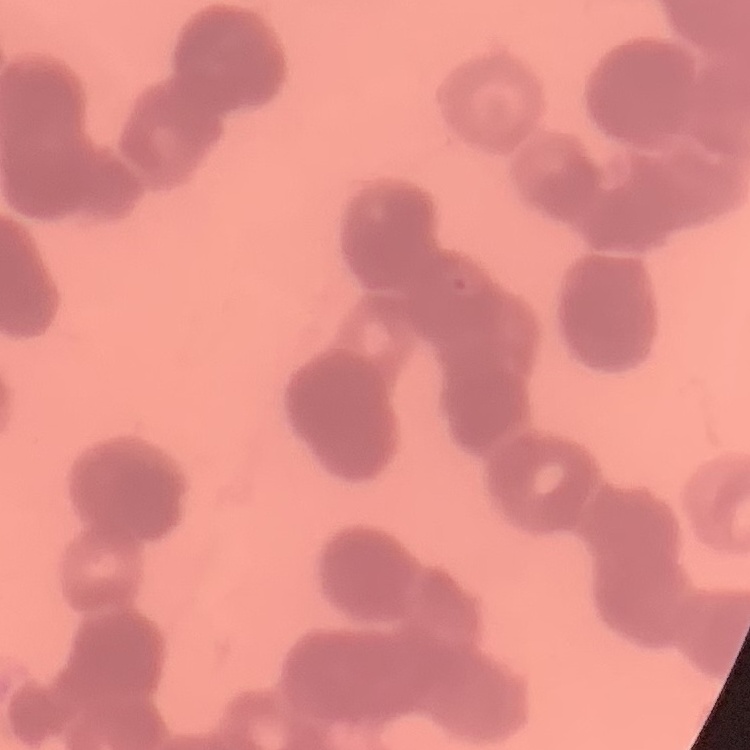
Summary:
  - Red blood cell morphology: rouleaux formation
  - Stain: Field's or Giemsa
  - Image type: square crop of a larger photomicrograph
  - Preparation: thin blood smear